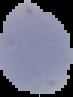
image type = segmented cell region with the area outside set to black
preparation = thin blood film
image size = 73×97 pixels
result = no Plasmodium parasites seen